Outline each blood parasite and name the species.
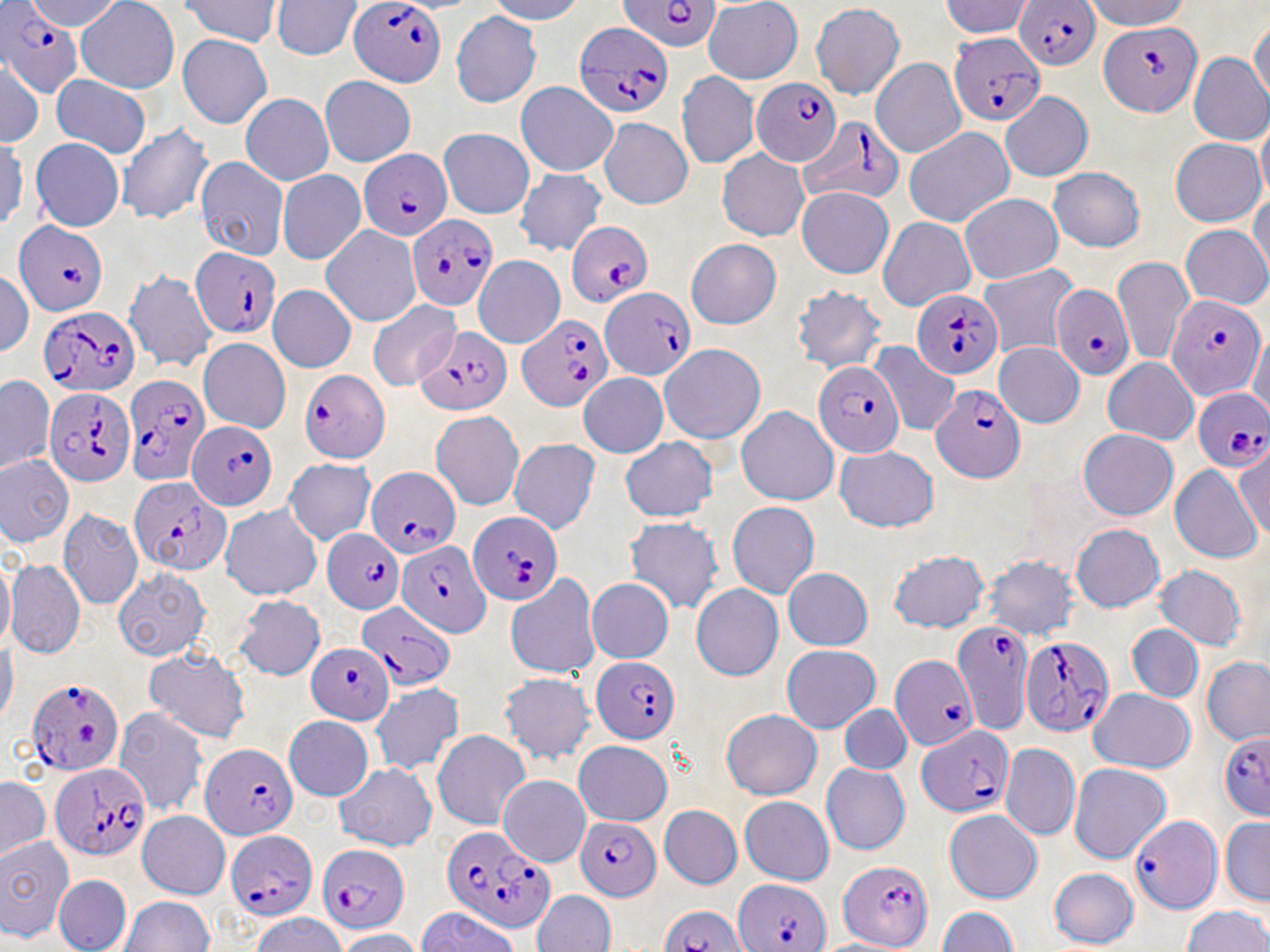

Approximate bounding boxes as (x1, y1, x2, y2) in pixels.
Plasmodium falciparum-infected red blood cells: (1017, 0, 1105, 67), (349, 1, 451, 84), (614, 1, 719, 54), (0, 2, 77, 98), (1100, 20, 1200, 113), (572, 21, 674, 116), (952, 34, 1049, 121), (752, 79, 840, 166), (800, 119, 905, 201), (357, 147, 453, 238), (406, 211, 495, 309), (13, 222, 108, 317), (568, 225, 651, 311), (192, 248, 283, 339), (1053, 285, 1132, 381), (600, 288, 696, 378), (912, 288, 1003, 380), (1168, 295, 1265, 399), (36, 302, 144, 392), (516, 315, 610, 411), (414, 327, 510, 414), (812, 358, 905, 458), (297, 367, 393, 461), (125, 376, 209, 479), (926, 376, 1030, 483), (44, 385, 137, 488), (1191, 389, 1270, 475), (189, 417, 276, 511), (367, 468, 460, 559), (125, 478, 234, 573), (468, 509, 560, 601), (326, 527, 405, 618), (398, 542, 492, 637), (358, 601, 455, 689), (952, 621, 1031, 729), (1019, 639, 1113, 738), (307, 645, 390, 725), (590, 654, 683, 742), (890, 655, 978, 750), (27, 680, 126, 777), (1215, 726, 1269, 825), (919, 728, 1017, 817), (200, 740, 297, 839), (48, 761, 154, 858), (573, 814, 659, 898), (1129, 815, 1222, 914), (437, 824, 552, 929), (225, 829, 317, 920), (320, 842, 408, 930), (833, 858, 934, 947), (729, 880, 832, 951), (658, 905, 743, 951).
No Plasmodium ovale, Plasmodium malariae, Plasmodium vivax, Babesia divergens, or Trypanosoma brucei observed.

Uninfected red blood cell locations: (77, 0, 180, 82), (274, 0, 362, 59), (179, 1, 285, 47), (937, 2, 1031, 37), (704, 4, 800, 83), (811, 4, 904, 98), (448, 10, 539, 108), (176, 32, 273, 126), (1186, 54, 1270, 143), (869, 58, 963, 157), (675, 69, 757, 170), (318, 74, 412, 166), (53, 76, 147, 157), (519, 84, 616, 176), (999, 96, 1092, 182), (242, 97, 331, 185), (597, 111, 693, 212), (117, 121, 214, 226), (442, 124, 533, 211), (906, 127, 1015, 228), (1169, 133, 1261, 225), (32, 135, 126, 231), (717, 147, 807, 242), (192, 154, 288, 258), (1049, 168, 1148, 251), (280, 170, 363, 262), (514, 170, 604, 256), (794, 191, 890, 277), (962, 195, 1067, 281), (880, 217, 978, 309), (319, 224, 421, 326), (1180, 227, 1268, 308), (685, 242, 781, 331), (472, 255, 564, 346), (1112, 258, 1191, 360), (974, 265, 1077, 353), (123, 270, 217, 369), (796, 284, 883, 371), (269, 286, 353, 371), (369, 300, 457, 389), (198, 339, 290, 431), (994, 344, 1081, 427), (660, 346, 765, 445), (1105, 360, 1167, 441), (578, 374, 665, 458), (0, 375, 53, 473), (737, 407, 838, 504), (431, 412, 525, 505), (1078, 426, 1177, 525), (622, 438, 712, 522), (513, 439, 598, 535), (836, 446, 933, 533), (0, 454, 72, 549), (285, 461, 375, 547), (1166, 465, 1260, 560), (219, 502, 321, 603), (729, 502, 814, 599), (60, 506, 143, 606), (626, 517, 719, 613), (1067, 519, 1165, 615), (887, 549, 988, 628), (984, 555, 1080, 640), (6, 557, 83, 660), (1155, 565, 1246, 650), (113, 567, 210, 664), (783, 570, 872, 646), (507, 574, 597, 677), (585, 580, 671, 661), (691, 583, 780, 679), (234, 594, 324, 681), (1126, 621, 1204, 701), (783, 646, 876, 732), (146, 649, 248, 741), (1203, 657, 1270, 740), (500, 676, 596, 763), (371, 682, 460, 774), (1088, 689, 1194, 773), (719, 706, 819, 798), (841, 706, 912, 771), (116, 710, 205, 814), (285, 716, 370, 802), (433, 730, 529, 831), (574, 740, 669, 821), (1002, 743, 1080, 839), (821, 760, 912, 855), (1069, 761, 1170, 860), (334, 762, 433, 850), (502, 775, 591, 864), (737, 791, 834, 883), (663, 805, 739, 886), (940, 806, 1040, 901), (138, 807, 228, 901), (1225, 819, 1270, 905), (0, 823, 66, 945), (1047, 866, 1142, 945), (53, 871, 128, 951), (532, 890, 613, 952), (121, 898, 214, 952), (937, 905, 1013, 952), (1184, 907, 1270, 952). Slide-level diagnosis: Plasmodium falciparum. May-Grünwald-Giemsa stain. 1000x magnification. Image is 1270×952 pixels. Single field of view. Light microscopy. Thin blood smear.